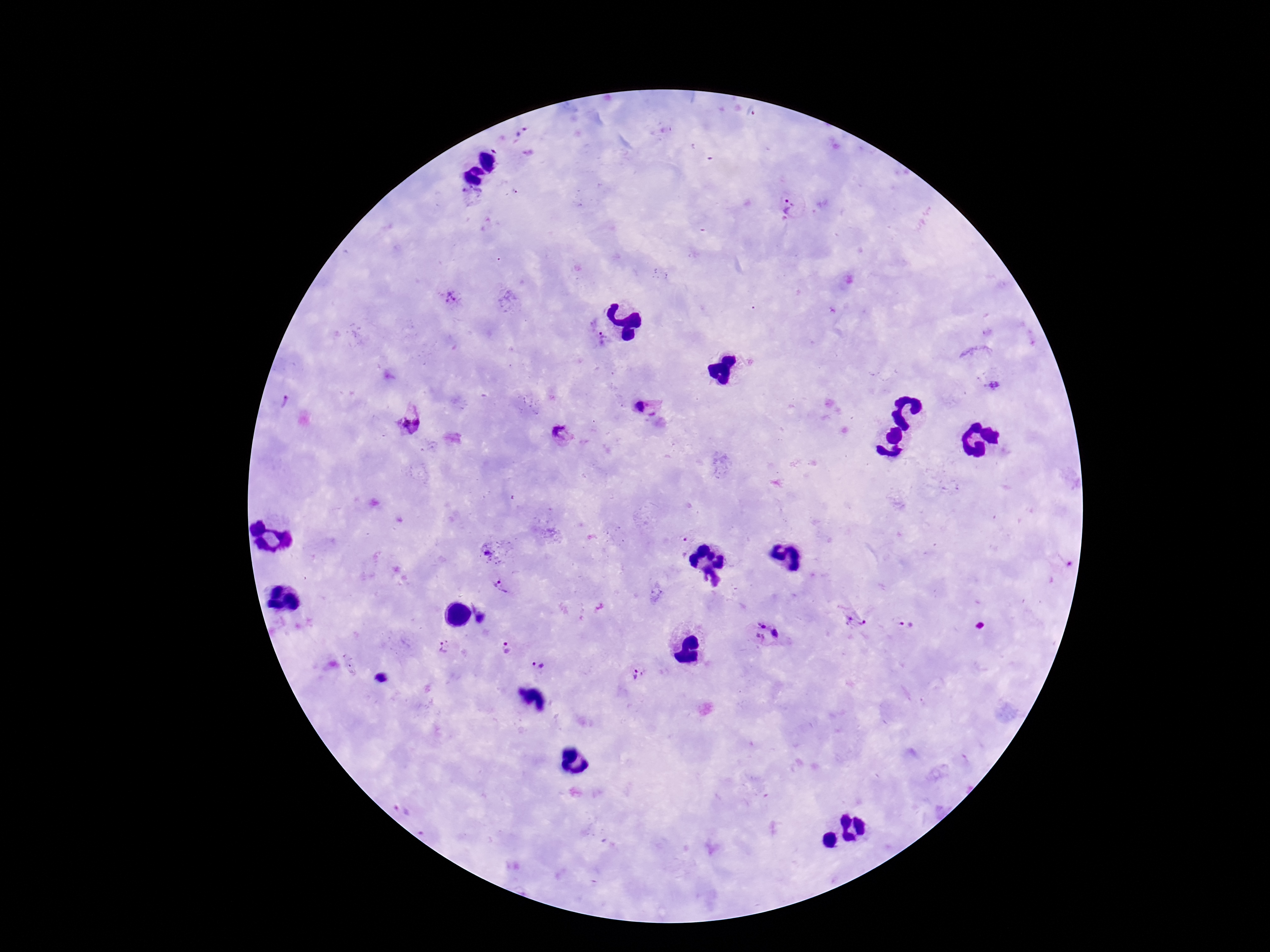

magnification = 100x
stain = Giemsa
capture = smartphone camera through the microscope eyepiece
Plasmodium parasite locations = approximate centers as {x, y} in pixels: {523, 133}, {472, 195}, {791, 209}, {451, 297}, {601, 339}, {995, 386}, {285, 404}, {641, 407}, {418, 422}, {405, 423}, {560, 432}, {681, 546}, {488, 554}, {501, 588}, {481, 618}, {856, 623}, {906, 624}, {761, 625}, {775, 633}, {760, 637}, {445, 647}, {506, 648}, {538, 665}, {639, 675}, {382, 679}, {403, 808}
field of view = one from this slide
patient malaria status = positive
image size = 1270×952 pixels
preparation = thick peripheral-blood smear